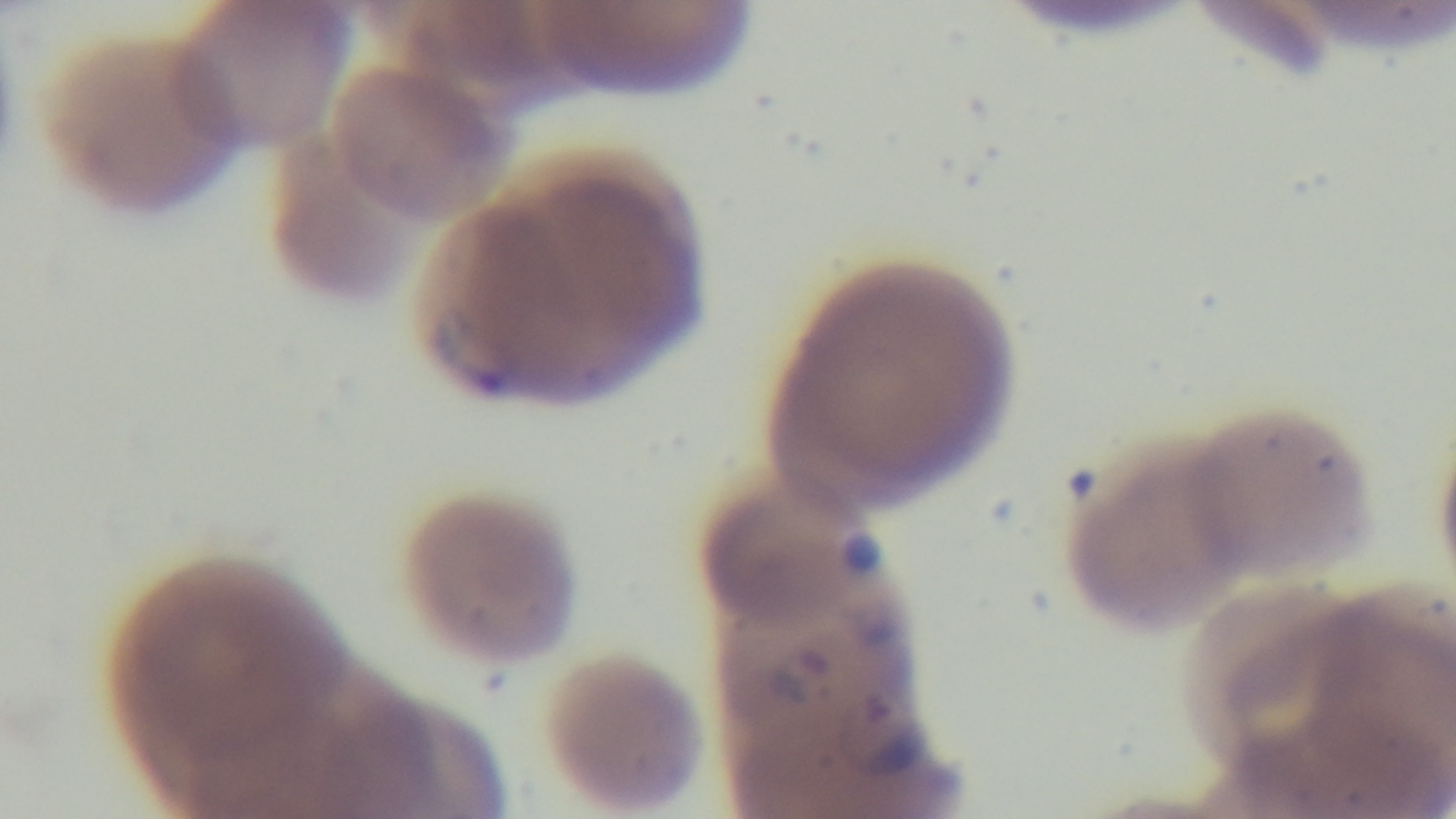 Photomicrograph. One field from the slide. Giemsa stain. Captured with a mounted 4K digital camera. Oil-immersion objective, 100x. Preparation: thin. Malaria status: positive.